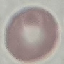
result = no malaria parasites detected
stain = Giemsa
image type = automatically extracted cell patch, resized to 64 × 64 pixels
preparation = thin blood smear
capture = smartphone camera at the microscope eyepiece